Find the cells and give the type of each one.
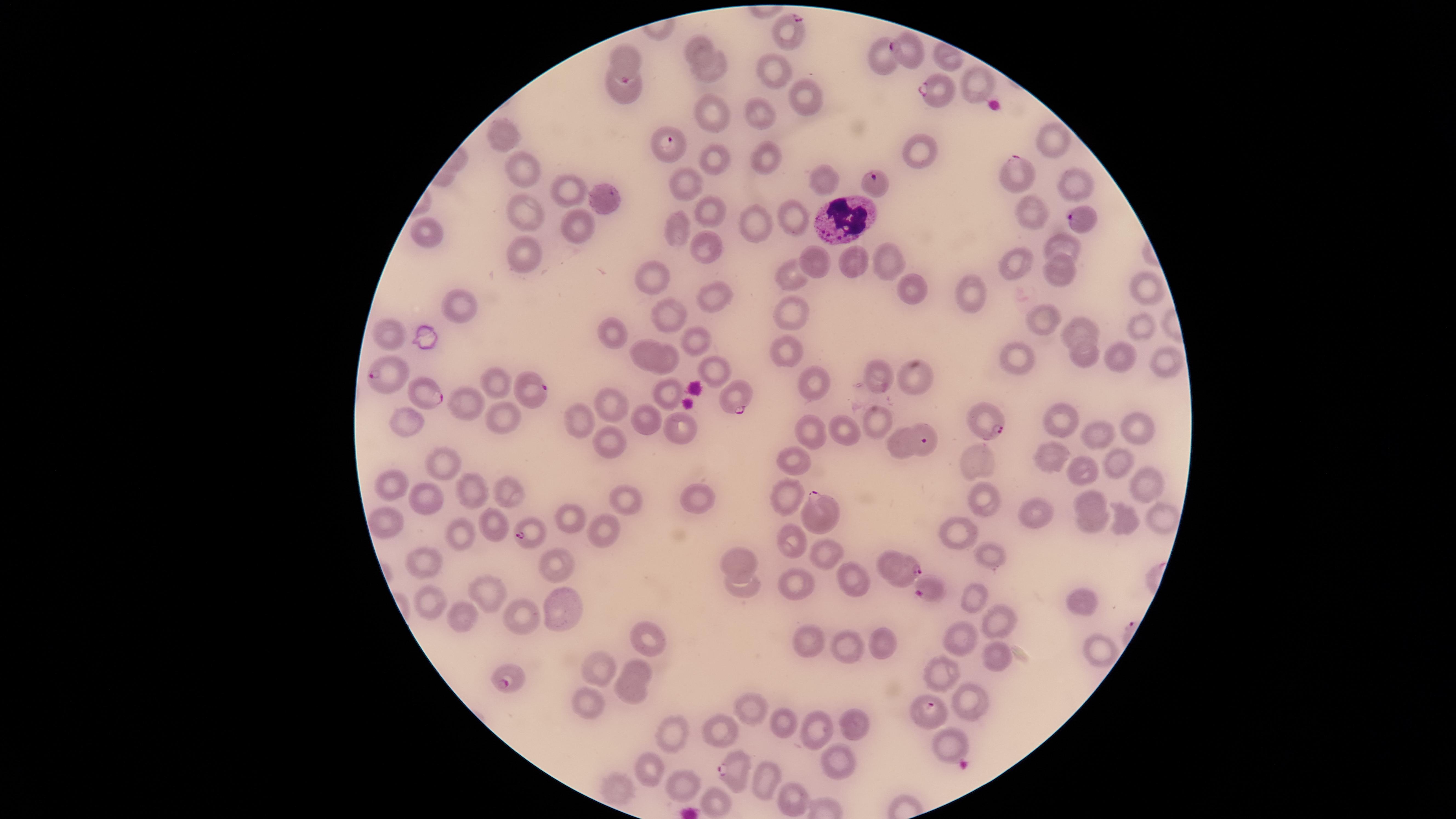
Approximate marker points as (x, y) in pixels.
Parasitized red blood cells: (788, 31), (907, 49), (624, 65), (935, 92), (669, 143), (1019, 177), (872, 181), (1081, 219), (382, 375), (529, 389), (420, 390), (733, 397), (990, 422), (922, 441), (821, 512), (531, 533), (903, 568), (930, 591), (509, 678), (926, 712), (734, 768).
Uninfected red blood cells: (698, 46), (942, 58), (881, 60), (707, 66), (774, 72), (970, 81), (621, 91), (802, 97), (710, 113), (758, 113), (499, 135), (1054, 139), (762, 156), (913, 157), (710, 160), (525, 164), (821, 178), (1070, 181), (684, 184), (568, 191), (600, 201), (524, 207), (707, 210), (1030, 211), (790, 220), (576, 225), (751, 225), (678, 231), (430, 234), (700, 244), (1059, 246), (523, 258), (884, 262), (817, 263), (853, 263), (1011, 268), (1062, 274), (789, 276), (655, 281), (908, 287), (1146, 288), (974, 296), (716, 299), (458, 302), (790, 315), (1038, 317), (668, 319), (1138, 325), (389, 330), (1084, 332), (609, 333), (696, 342), (787, 354), (643, 355), (1084, 358), (1122, 358), (668, 359), (1015, 360), (1161, 360), (716, 368), (879, 378), (496, 381), (815, 381), (915, 381), (673, 392), (464, 400), (611, 402), (648, 417), (505, 419), (876, 420), (1064, 421), (402, 423), (581, 425), (680, 427), (839, 429), (1131, 429), (808, 430), (1093, 440), (607, 443), (901, 443), (1049, 456), (791, 462), (1116, 462), (972, 463), (445, 466), (1082, 475), (1142, 483), (392, 485), (509, 490), (473, 494), (782, 495), (429, 498), (623, 499), (697, 500), (988, 500), (1086, 500), (566, 514), (1041, 516), (1166, 521), (1090, 522), (391, 523), (488, 524), (1125, 524), (602, 531), (957, 535), (461, 536), (792, 545), (822, 553), (987, 559), (887, 560), (424, 562), (557, 562), (740, 562), (853, 581), (795, 585), (741, 586), (490, 591), (972, 597), (433, 601), (1076, 602), (562, 609), (527, 616), (464, 617), (995, 623), (643, 637), (958, 640), (808, 641), (880, 641), (844, 649), (995, 652), (1101, 652), (601, 668), (637, 672), (942, 676), (632, 692), (593, 704), (967, 706), (749, 708), (853, 725), (784, 728), (722, 730), (811, 732), (674, 735), (948, 739), (836, 767), (647, 772), (767, 778), (679, 783), (617, 791), (716, 800), (792, 800).
White blood cells: (845, 221).

Giemsa-stained preparation. Thin blood smear. Image is 1456×819 pixels. Circular visible region. Photographed with a smartphone camera through the microscope eyepiece. Species: Plasmodium falciparum. Single field of view.